Report the malaria status of this cell.
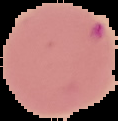
Parasitized.

{
  "preparation": "thin blood smear",
  "image_size": "118×121 pixels",
  "image_type": "segmented cell region with the area outside set to black"
}